Outline each Plasmodium falciparum-infected red blood cell.
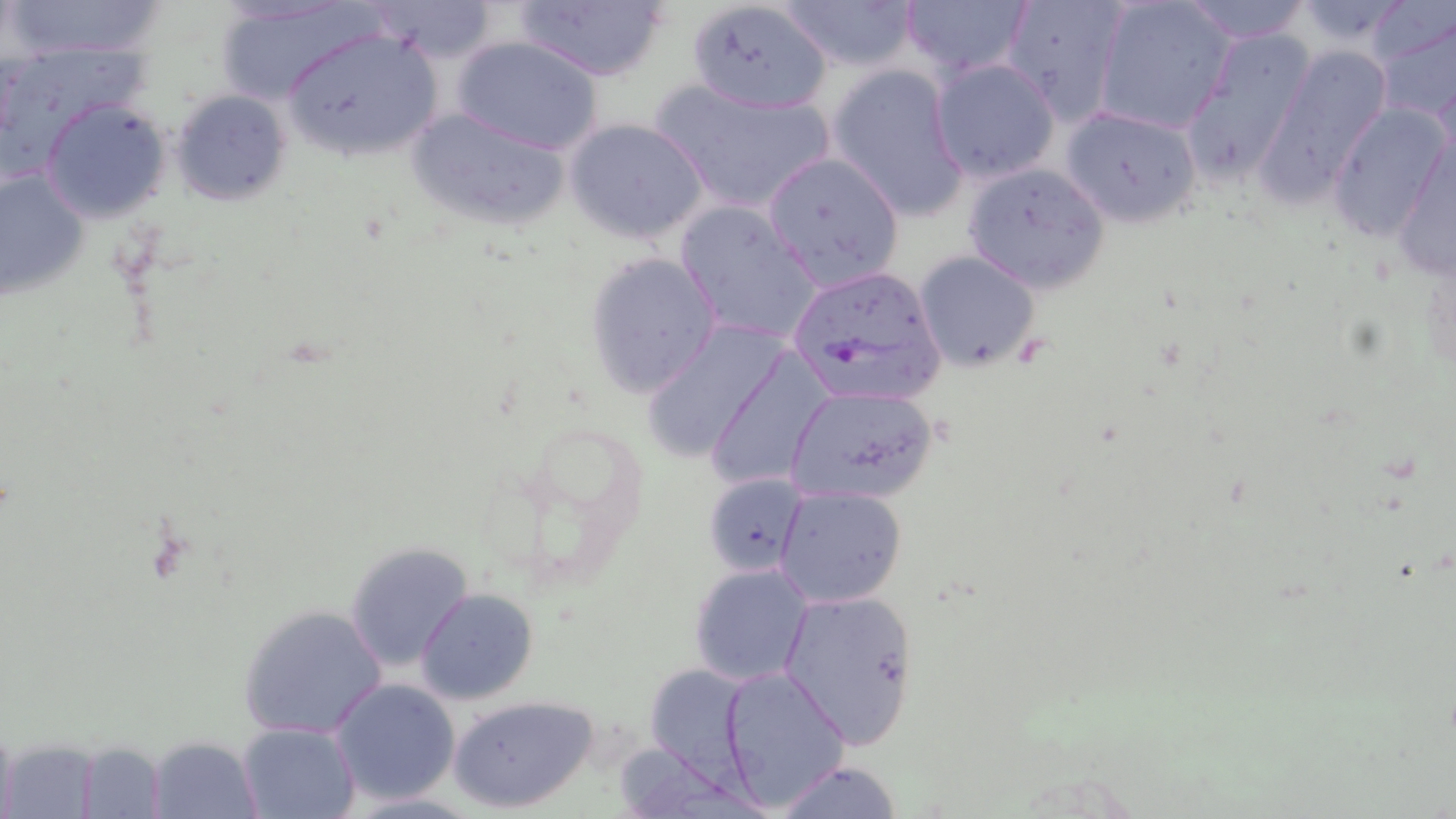

Approximate bounding boxes as (x1,y1)-(x2,y2) corner pairs in pixels.
Plasmodium falciparum-infected red blood cells: (784,264)-(947,408).

Uninfected red blood cell locations: (7,0)-(171,62), (212,0)-(376,107), (363,0)-(500,65), (512,0)-(670,83), (685,0)-(834,114), (777,0)-(920,73), (897,0)-(1033,80), (1000,0)-(1130,122), (1092,0)-(1235,136), (1178,1)-(1315,44), (1289,1)-(1421,52), (1372,10)-(1456,128), (279,25)-(445,164), (1180,28)-(1315,189), (454,36)-(603,153), (1259,44)-(1393,197), (929,58)-(1061,182), (827,65)-(969,223), (650,78)-(839,216), (170,90)-(292,205), (41,99)-(170,221), (1328,103)-(1451,242), (405,104)-(571,231), (1060,104)-(1202,228), (566,117)-(710,245), (1389,130)-(1455,287), (762,151)-(904,289), (963,162)-(1109,293), (0,165)-(90,301), (674,200)-(824,348), (583,250)-(722,398), (914,251)-(1040,370), (639,320)-(793,463), (704,346)-(836,492), (781,385)-(940,505), (702,473)-(807,576), (775,485)-(908,609), (344,541)-(473,671), (688,562)-(815,686), (415,588)-(539,705), (778,588)-(919,748), (236,603)-(389,742), (643,661)-(756,781), (720,665)-(850,809), (330,678)-(460,805), (449,694)-(598,813), (238,721)-(362,818), (145,734)-(263,818), (4,738)-(101,816), (76,740)-(169,817), (771,759)-(906,819). Slide-level diagnosis: Plasmodium falciparum. Captured at 1000x magnification. Optical microscopy. Single field of view. Image is 1456×819 pixels. May-Grünwald-Giemsa stain. Thin blood smear.